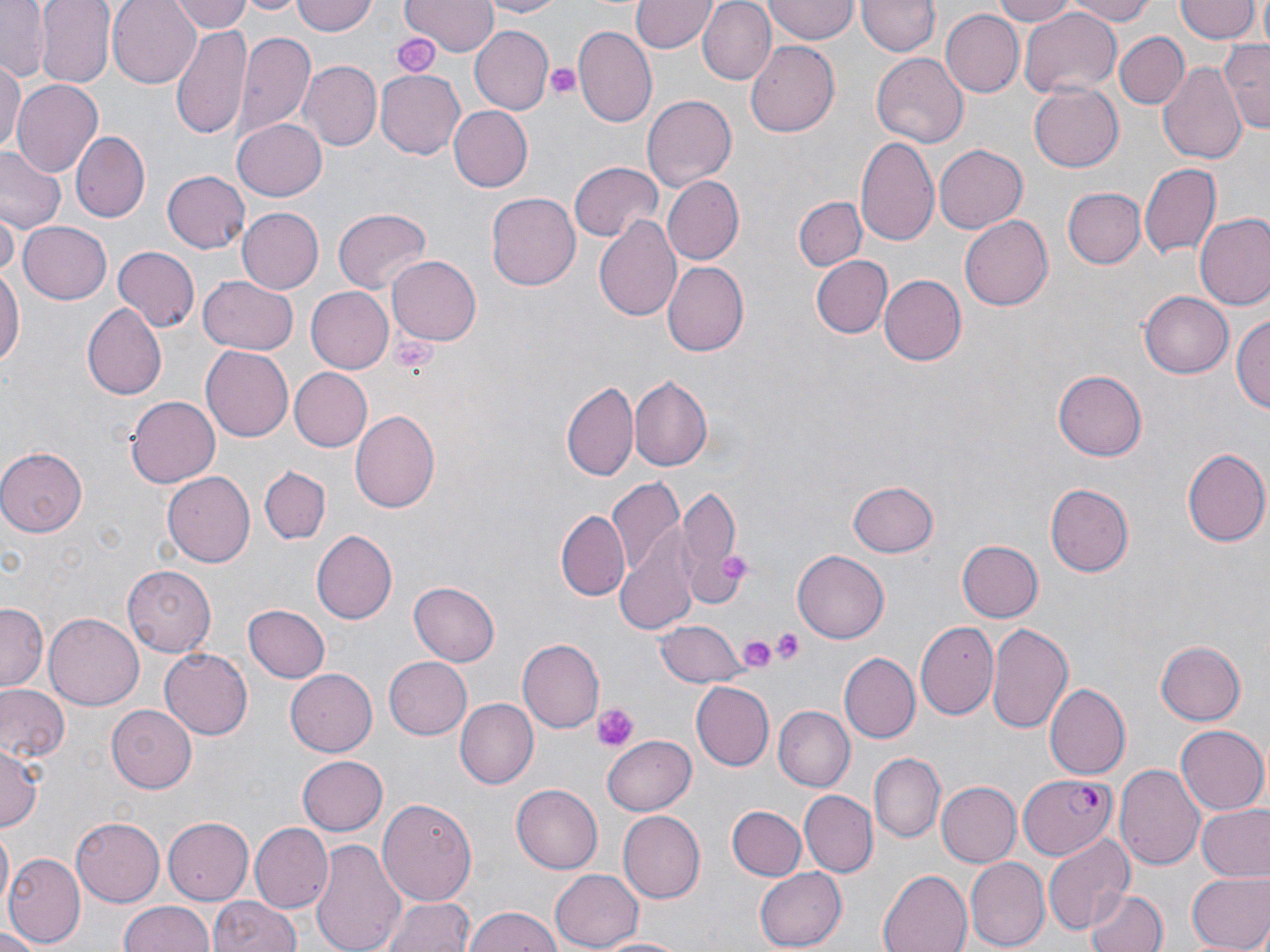
Approximate bounding boxes as named x1/y1/x2/y2 corners in pixels. Plasmodium falciparum-infected red blood cell locations: (x1=1018, y1=773, x2=1119, y2=861). Uninfected red blood cell locations: (x1=33, y1=0, x2=115, y2=88), (x1=105, y1=0, x2=201, y2=87), (x1=171, y1=0, x2=257, y2=33), (x1=240, y1=0, x2=303, y2=16), (x1=293, y1=0, x2=378, y2=36), (x1=402, y1=0, x2=496, y2=55), (x1=478, y1=0, x2=566, y2=17), (x1=632, y1=0, x2=716, y2=54), (x1=698, y1=0, x2=776, y2=84), (x1=764, y1=0, x2=859, y2=42), (x1=859, y1=0, x2=938, y2=57), (x1=989, y1=0, x2=1081, y2=25), (x1=1059, y1=0, x2=1159, y2=25), (x1=1175, y1=1, x2=1259, y2=44), (x1=0, y1=3, x2=52, y2=78), (x1=1021, y1=8, x2=1122, y2=100), (x1=939, y1=9, x2=1022, y2=99), (x1=171, y1=25, x2=252, y2=139), (x1=572, y1=25, x2=656, y2=127), (x1=472, y1=26, x2=553, y2=114), (x1=237, y1=30, x2=317, y2=139), (x1=1114, y1=31, x2=1189, y2=109), (x1=1220, y1=38, x2=1270, y2=134), (x1=745, y1=40, x2=843, y2=137), (x1=871, y1=51, x2=970, y2=146), (x1=1157, y1=57, x2=1246, y2=163), (x1=301, y1=60, x2=382, y2=152), (x1=0, y1=61, x2=22, y2=156), (x1=374, y1=69, x2=464, y2=159), (x1=11, y1=77, x2=102, y2=175), (x1=1026, y1=82, x2=1122, y2=173), (x1=642, y1=93, x2=736, y2=189), (x1=446, y1=105, x2=532, y2=193), (x1=232, y1=117, x2=328, y2=201), (x1=70, y1=131, x2=149, y2=221), (x1=855, y1=136, x2=940, y2=246), (x1=932, y1=144, x2=1025, y2=234), (x1=0, y1=146, x2=64, y2=233), (x1=569, y1=159, x2=662, y2=242), (x1=1139, y1=164, x2=1220, y2=259), (x1=163, y1=169, x2=250, y2=253), (x1=661, y1=176, x2=744, y2=264), (x1=1063, y1=188, x2=1146, y2=269), (x1=486, y1=193, x2=580, y2=292), (x1=795, y1=195, x2=866, y2=270), (x1=235, y1=207, x2=323, y2=295), (x1=330, y1=207, x2=431, y2=297), (x1=1, y1=210, x2=18, y2=280), (x1=595, y1=212, x2=682, y2=323), (x1=1195, y1=214, x2=1270, y2=312), (x1=961, y1=216, x2=1053, y2=310), (x1=17, y1=220, x2=112, y2=305), (x1=114, y1=246, x2=199, y2=331), (x1=388, y1=255, x2=481, y2=346), (x1=808, y1=255, x2=893, y2=340), (x1=661, y1=261, x2=748, y2=357), (x1=0, y1=265, x2=24, y2=372), (x1=198, y1=275, x2=298, y2=355), (x1=879, y1=275, x2=966, y2=365), (x1=306, y1=287, x2=396, y2=374), (x1=1139, y1=290, x2=1232, y2=378), (x1=80, y1=301, x2=167, y2=400), (x1=1233, y1=309, x2=1270, y2=418), (x1=199, y1=345, x2=293, y2=442), (x1=287, y1=368, x2=371, y2=451), (x1=1054, y1=371, x2=1147, y2=460), (x1=630, y1=376, x2=713, y2=471), (x1=562, y1=380, x2=639, y2=482), (x1=125, y1=396, x2=220, y2=487), (x1=350, y1=410, x2=440, y2=512), (x1=1182, y1=445, x2=1269, y2=548), (x1=0, y1=448, x2=84, y2=536), (x1=258, y1=465, x2=331, y2=543), (x1=163, y1=473, x2=254, y2=566), (x1=606, y1=479, x2=684, y2=587), (x1=847, y1=480, x2=939, y2=558), (x1=1046, y1=482, x2=1134, y2=577), (x1=678, y1=486, x2=747, y2=605), (x1=556, y1=511, x2=630, y2=599), (x1=613, y1=523, x2=702, y2=638), (x1=313, y1=531, x2=397, y2=624), (x1=957, y1=540, x2=1043, y2=623), (x1=793, y1=549, x2=890, y2=642), (x1=123, y1=566, x2=216, y2=654), (x1=409, y1=580, x2=500, y2=666), (x1=0, y1=604, x2=45, y2=693), (x1=244, y1=604, x2=331, y2=682), (x1=42, y1=613, x2=143, y2=711), (x1=656, y1=619, x2=746, y2=688), (x1=986, y1=620, x2=1073, y2=735), (x1=916, y1=622, x2=1000, y2=720), (x1=518, y1=637, x2=603, y2=733), (x1=1153, y1=640, x2=1245, y2=727), (x1=160, y1=649, x2=253, y2=738), (x1=839, y1=654, x2=919, y2=743), (x1=383, y1=657, x2=472, y2=740), (x1=284, y1=670, x2=376, y2=755), (x1=693, y1=682, x2=773, y2=771), (x1=0, y1=683, x2=69, y2=766), (x1=1043, y1=683, x2=1130, y2=779), (x1=455, y1=698, x2=538, y2=789), (x1=107, y1=704, x2=197, y2=793), (x1=774, y1=706, x2=853, y2=790), (x1=1176, y1=724, x2=1268, y2=814), (x1=601, y1=735, x2=696, y2=816), (x1=0, y1=745, x2=42, y2=832), (x1=871, y1=752, x2=944, y2=841), (x1=297, y1=755, x2=388, y2=836), (x1=1116, y1=763, x2=1207, y2=872), (x1=934, y1=781, x2=1019, y2=869), (x1=512, y1=786, x2=602, y2=872), (x1=799, y1=790, x2=875, y2=879), (x1=379, y1=796, x2=477, y2=910), (x1=727, y1=805, x2=806, y2=880), (x1=1197, y1=805, x2=1270, y2=880), (x1=616, y1=810, x2=704, y2=902), (x1=165, y1=816, x2=254, y2=903), (x1=72, y1=818, x2=165, y2=905), (x1=249, y1=822, x2=334, y2=913), (x1=1, y1=828, x2=13, y2=912), (x1=1041, y1=831, x2=1135, y2=938), (x1=311, y1=836, x2=406, y2=952), (x1=4, y1=852, x2=83, y2=946), (x1=965, y1=856, x2=1049, y2=950), (x1=550, y1=868, x2=642, y2=949), (x1=755, y1=868, x2=846, y2=948), (x1=878, y1=868, x2=972, y2=952), (x1=1184, y1=870, x2=1270, y2=952), (x1=1085, y1=886, x2=1166, y2=952), (x1=379, y1=894, x2=475, y2=952), (x1=210, y1=895, x2=300, y2=952), (x1=118, y1=900, x2=217, y2=952), (x1=463, y1=908, x2=567, y2=952), (x1=0, y1=926, x2=48, y2=952), (x1=593, y1=934, x2=691, y2=951). Platelet locations: (x1=391, y1=31, x2=439, y2=77), (x1=543, y1=61, x2=581, y2=103), (x1=391, y1=334, x2=434, y2=375), (x1=718, y1=552, x2=754, y2=585), (x1=773, y1=627, x2=807, y2=665), (x1=733, y1=632, x2=780, y2=675), (x1=595, y1=703, x2=637, y2=749). Slide-level diagnosis: Plasmodium falciparum. Image is 1270×952 pixels. Single field of view. Captured at 1000x magnification. Thin blood film. May-Grünwald-Giemsa stain. Optical microscopy.